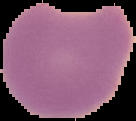

Result: malaria parasites identified. Segmented cell region on a black background. From a thin blood smear. Image is 136×121 pixels.